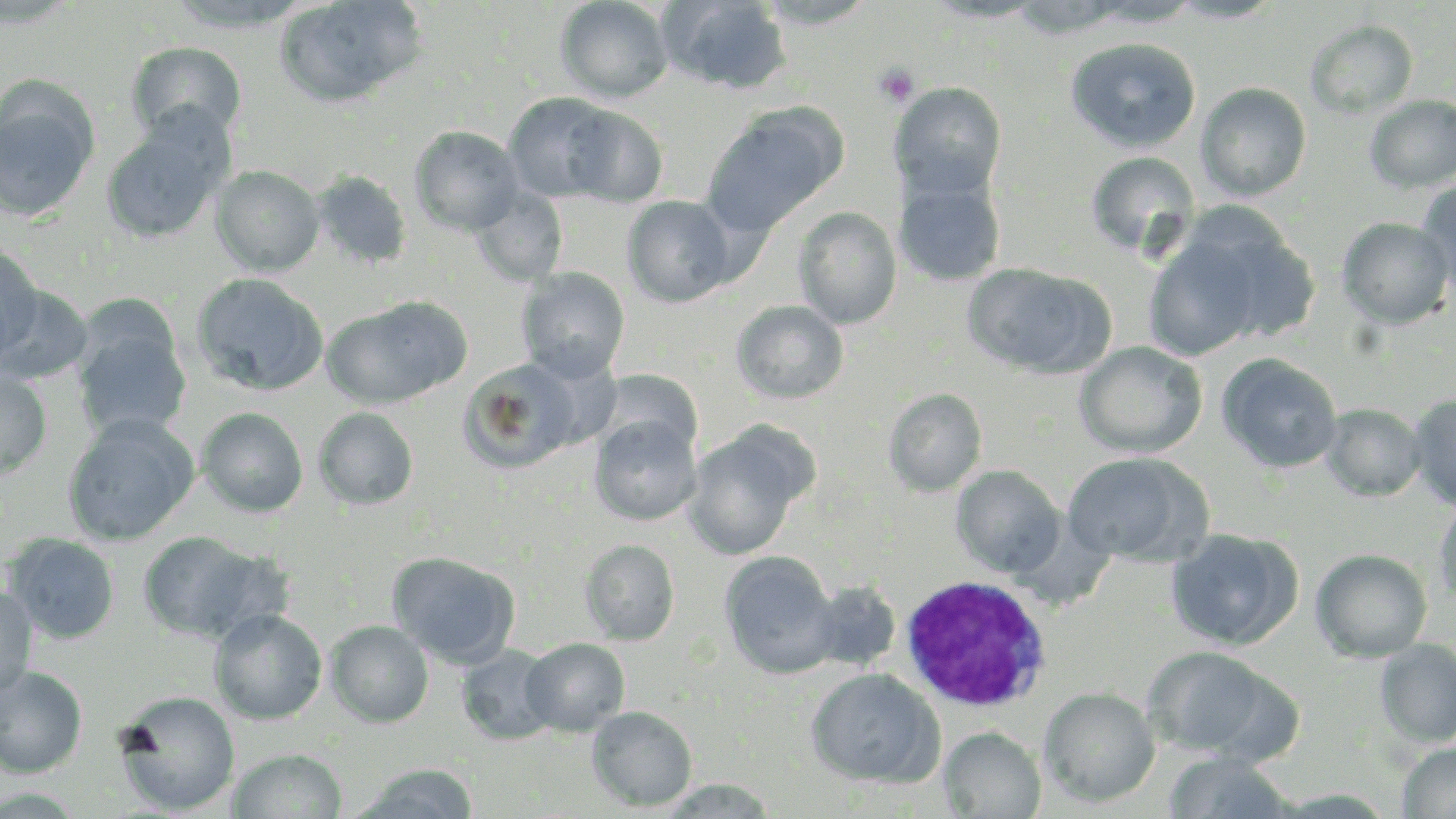

slide-level diagnosis = Plasmodium ovale
uninfected red blood cell locations = approximate bounding boxes as named x1/y1/x2/y2 corners in pixels: (x1=274, y1=0, x2=426, y2=108), (x1=555, y1=0, x2=674, y2=103), (x1=660, y1=0, x2=792, y2=93), (x1=165, y1=1, x2=316, y2=33), (x1=753, y1=1, x2=880, y2=29), (x1=921, y1=1, x2=1048, y2=23), (x1=1083, y1=1, x2=1202, y2=27), (x1=1168, y1=1, x2=1285, y2=24), (x1=1304, y1=19, x2=1418, y2=118), (x1=1065, y1=37, x2=1201, y2=153), (x1=126, y1=41, x2=247, y2=144), (x1=891, y1=82, x2=1007, y2=199), (x1=1196, y1=82, x2=1311, y2=201), (x1=0, y1=85, x2=100, y2=225), (x1=504, y1=92, x2=622, y2=203), (x1=1364, y1=95, x2=1456, y2=193), (x1=564, y1=105, x2=668, y2=207), (x1=702, y1=107, x2=842, y2=237), (x1=100, y1=119, x2=228, y2=245), (x1=409, y1=126, x2=525, y2=236), (x1=1086, y1=151, x2=1201, y2=258), (x1=211, y1=165, x2=324, y2=277), (x1=310, y1=170, x2=413, y2=271), (x1=893, y1=175, x2=1006, y2=286), (x1=1416, y1=180, x2=1456, y2=293), (x1=470, y1=187, x2=568, y2=286), (x1=622, y1=195, x2=736, y2=308), (x1=793, y1=207, x2=902, y2=329), (x1=1146, y1=214, x2=1312, y2=361), (x1=1337, y1=217, x2=1455, y2=329), (x1=0, y1=243, x2=43, y2=365), (x1=963, y1=262, x2=1115, y2=380), (x1=516, y1=268, x2=629, y2=383), (x1=191, y1=272, x2=329, y2=396), (x1=1, y1=284, x2=95, y2=385), (x1=322, y1=299, x2=467, y2=409), (x1=732, y1=299, x2=849, y2=404), (x1=72, y1=321, x2=190, y2=438), (x1=1075, y1=341, x2=1207, y2=458), (x1=1216, y1=352, x2=1344, y2=473), (x1=458, y1=357, x2=584, y2=474), (x1=597, y1=369, x2=701, y2=459), (x1=0, y1=370, x2=53, y2=482), (x1=884, y1=387, x2=987, y2=497), (x1=1409, y1=394, x2=1456, y2=511), (x1=1321, y1=403, x2=1427, y2=501), (x1=197, y1=406, x2=308, y2=517), (x1=313, y1=407, x2=419, y2=510), (x1=62, y1=414, x2=199, y2=546), (x1=589, y1=415, x2=701, y2=526), (x1=681, y1=426, x2=810, y2=562), (x1=1060, y1=451, x2=1207, y2=564), (x1=952, y1=465, x2=1066, y2=579), (x1=1432, y1=497, x2=1456, y2=611), (x1=1166, y1=528, x2=1301, y2=651), (x1=136, y1=530, x2=273, y2=643), (x1=2, y1=532, x2=121, y2=645), (x1=579, y1=539, x2=680, y2=646), (x1=1310, y1=548, x2=1433, y2=662), (x1=388, y1=551, x2=520, y2=670), (x1=720, y1=551, x2=839, y2=678), (x1=805, y1=581, x2=902, y2=672), (x1=0, y1=587, x2=39, y2=699), (x1=209, y1=608, x2=328, y2=724), (x1=326, y1=620, x2=434, y2=728), (x1=522, y1=638, x2=630, y2=736), (x1=1375, y1=639, x2=1456, y2=748), (x1=457, y1=644, x2=560, y2=745), (x1=1144, y1=646, x2=1276, y2=758), (x1=0, y1=665, x2=88, y2=778), (x1=805, y1=668, x2=943, y2=787), (x1=0, y1=671, x2=182, y2=788), (x1=1039, y1=687, x2=1160, y2=808), (x1=113, y1=690, x2=240, y2=815), (x1=587, y1=707, x2=697, y2=811), (x1=939, y1=727, x2=1046, y2=818), (x1=1398, y1=742, x2=1456, y2=818), (x1=228, y1=748, x2=348, y2=818), (x1=1164, y1=751, x2=1299, y2=817), (x1=350, y1=763, x2=481, y2=818), (x1=656, y1=778, x2=780, y2=817), (x1=1272, y1=788, x2=1398, y2=818)
platelet locations = approximate bounding boxes as named x1/y1/x2/y2 corners in pixels: (x1=874, y1=62, x2=921, y2=107)
image size = 1456×819 pixels
preparation = thin blood film
magnification = 1000x
stain = May-Grünwald-Giemsa
white blood cell locations = approximate bounding boxes as named x1/y1/x2/y2 corners in pixels: (x1=897, y1=574, x2=1055, y2=712)
field of view = one of a larger specimen
modality = optical microscopy